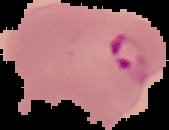

Summary:
  - Image type: segmented cell region on a black background
  - Malaria status: parasitized
  - Image size: 169×130 pixels
  - Preparation: thin blood film